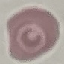
Summary:
  - Result: negative for malaria parasites
  - Stain: Giemsa
  - Preparation: thin blood film
  - Image type: cell patch, automatically extracted from a larger field of view and resized to 64 × 64 pixels
  - Capture: smartphone through the microscope eyepiece